Comment on the morphology of the red blood cells.
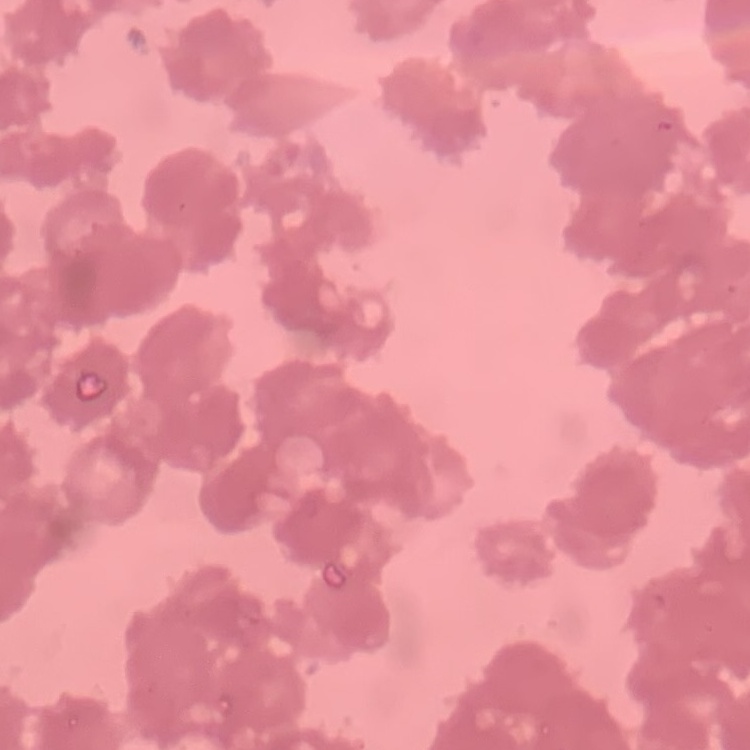
They show rouleaux formation.

stain = Field's or Giemsa
image type = square crop of a larger photomicrograph
preparation = thin blood smear